Name the parasite shown.
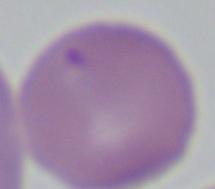

This is Babesia.

modality: micrograph
magnification: 1000x